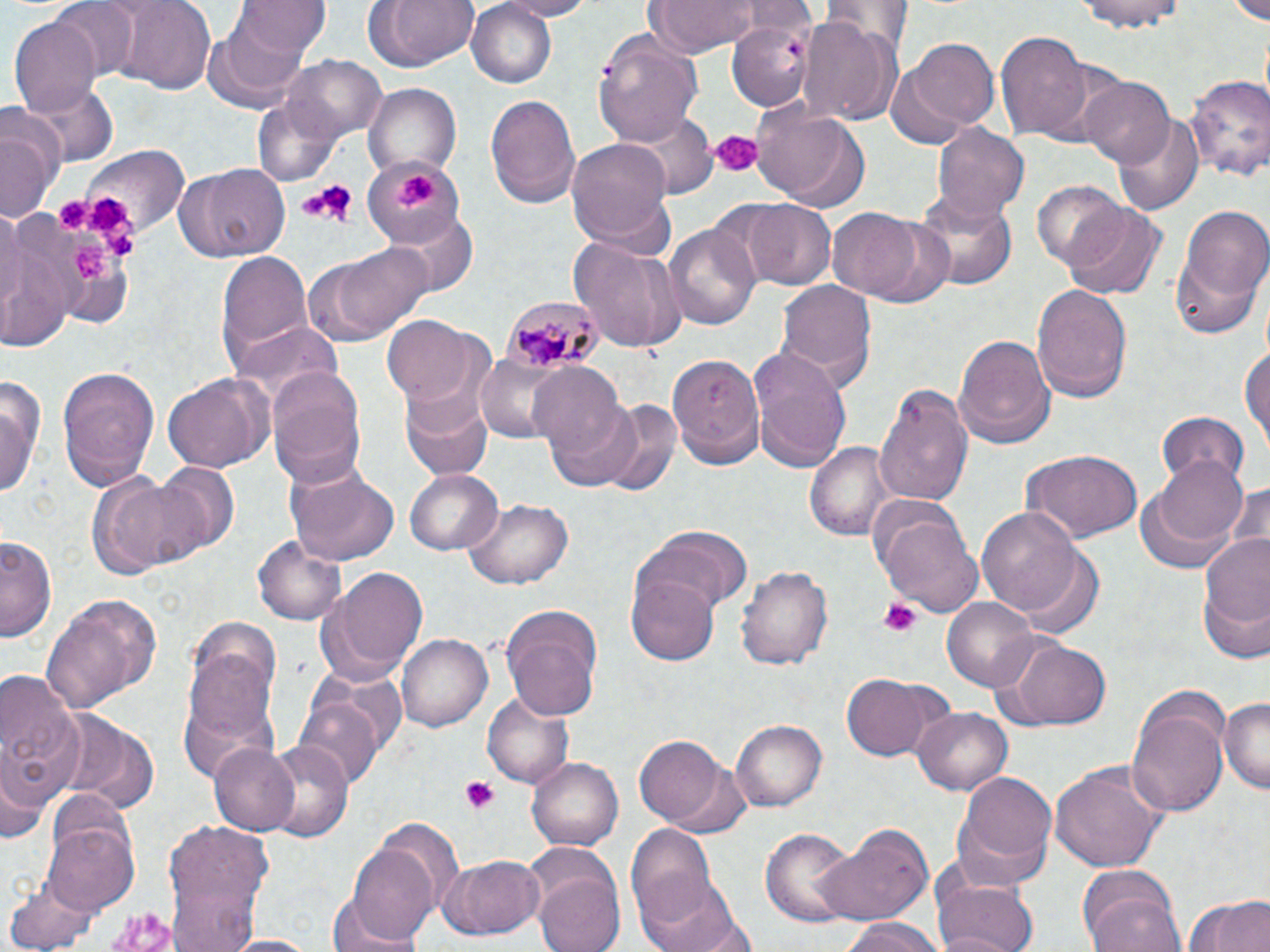

Summary:
  - Coordinate format: approximate bounding boxes as (x1,y1)-(x2,y2) corner pairs in pixels
  - Platelet locations: (709,131)-(760,176), (396,173)-(435,210), (296,178)-(354,226), (91,195)-(131,238), (54,197)-(89,231), (103,234)-(148,264), (74,243)-(119,283), (879,597)-(922,635), (460,776)-(502,815)
  - Uninfected red blood cell locations: (49,0)-(143,80), (104,0)-(218,92), (362,0)-(479,72), (493,0)-(600,19), (647,0)-(767,56), (1074,0)-(1187,32), (234,1)-(330,60), (817,1)-(913,62), (1231,1)-(1270,24), (466,2)-(558,88), (9,13)-(103,120), (799,16)-(901,127), (203,20)-(314,112), (728,22)-(815,110), (596,30)-(705,145), (996,30)-(1095,143), (906,37)-(998,132), (285,54)-(386,141), (885,64)-(973,148), (1182,73)-(1269,183), (1080,76)-(1175,165), (21,80)-(116,167), (364,81)-(464,178), (251,93)-(344,188), (484,93)-(580,208), (752,105)-(871,209), (629,112)-(715,199), (0,114)-(57,225), (1115,115)-(1204,217), (930,122)-(1030,220), (568,140)-(676,249), (83,143)-(191,240), (364,154)-(462,248), (173,162)-(292,263), (1031,182)-(1134,277), (917,188)-(1015,291), (736,198)-(838,290), (1061,203)-(1166,302), (1173,205)-(1269,331), (825,206)-(943,305), (388,211)-(478,297), (0,222)-(78,351), (664,222)-(763,331), (569,237)-(685,356), (301,242)-(432,347), (214,252)-(312,369), (776,277)-(878,394), (1030,284)-(1131,403), (382,317)-(483,408), (229,320)-(343,404), (954,334)-(1055,449), (749,342)-(852,469), (1242,345)-(1269,450), (669,354)-(764,469), (474,357)-(572,441), (528,363)-(632,471), (57,365)-(160,489), (268,370)-(367,486), (0,373)-(43,500), (162,373)-(275,473), (874,382)-(972,508), (400,388)-(496,480), (544,394)-(651,493), (601,403)-(682,495), (1155,412)-(1251,491), (804,440)-(894,542), (1020,449)-(1143,545), (1152,456)-(1251,548), (151,461)-(240,555), (286,464)-(398,565), (404,470)-(503,556), (86,471)-(207,579), (1224,477)-(1269,555), (1134,480)-(1242,578), (462,497)-(574,589), (977,508)-(1084,618), (878,511)-(983,619), (641,522)-(754,614), (1195,526)-(1270,656), (2,534)-(59,644), (255,535)-(349,625), (1013,549)-(1104,639), (738,565)-(833,671), (320,567)-(429,683), (628,567)-(719,666), (40,594)-(161,714), (942,597)-(1040,693), (500,605)-(602,718), (399,635)-(492,731), (995,638)-(1113,730), (180,640)-(280,769), (0,669)-(87,807), (845,674)-(935,760), (483,693)-(573,787), (298,695)-(385,791), (1124,696)-(1229,820), (1217,696)-(1270,793), (913,707)-(1012,793), (59,712)-(161,813), (731,720)-(827,810), (636,735)-(734,829), (259,739)-(354,844), (209,743)-(303,834), (528,757)-(623,852), (0,761)-(48,848), (1048,761)-(1168,872), (950,775)-(1055,887), (42,816)-(140,917), (374,817)-(464,911), (160,819)-(278,952), (629,824)-(717,925), (819,826)-(933,928), (763,827)-(860,929), (343,843)-(439,948), (440,855)-(545,940), (930,867)-(1040,952), (533,871)-(625,952), (640,875)-(743,952), (1077,876)-(1185,952), (3,879)-(100,952), (1181,893)-(1270,952), (326,899)-(431,952), (841,920)-(947,952), (224,933)-(315,952)
  - Plasmodium malariae-infected red blood cell locations: (501,296)-(600,373)
  - Slide-level diagnosis: Plasmodium malariae
  - Image size: 1270×952 pixels
  - Preparation: thin blood smear
  - Field of view: single
  - Modality: light microscopy
  - Stain: May-Grünwald-Giemsa
  - Magnification: 1000x